Assess this cell for malaria.
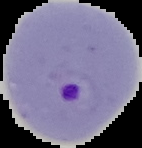
Parasitized.

image size = 142×148 pixels
preparation = thin blood film
image type = segmented cell region on a black background